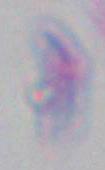

Summary:
  - Identification: Toxoplasma gondii
  - Modality: micrograph
  - Magnification: 1000x